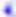
magnification: 400x
identification: Toxoplasma gondii
modality: photomicrograph